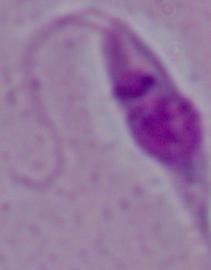

Summary:
  - Identification: Leishmania
  - Modality: photomicrograph
  - Magnification: 1000x